Outline each blood parasite and name the species.
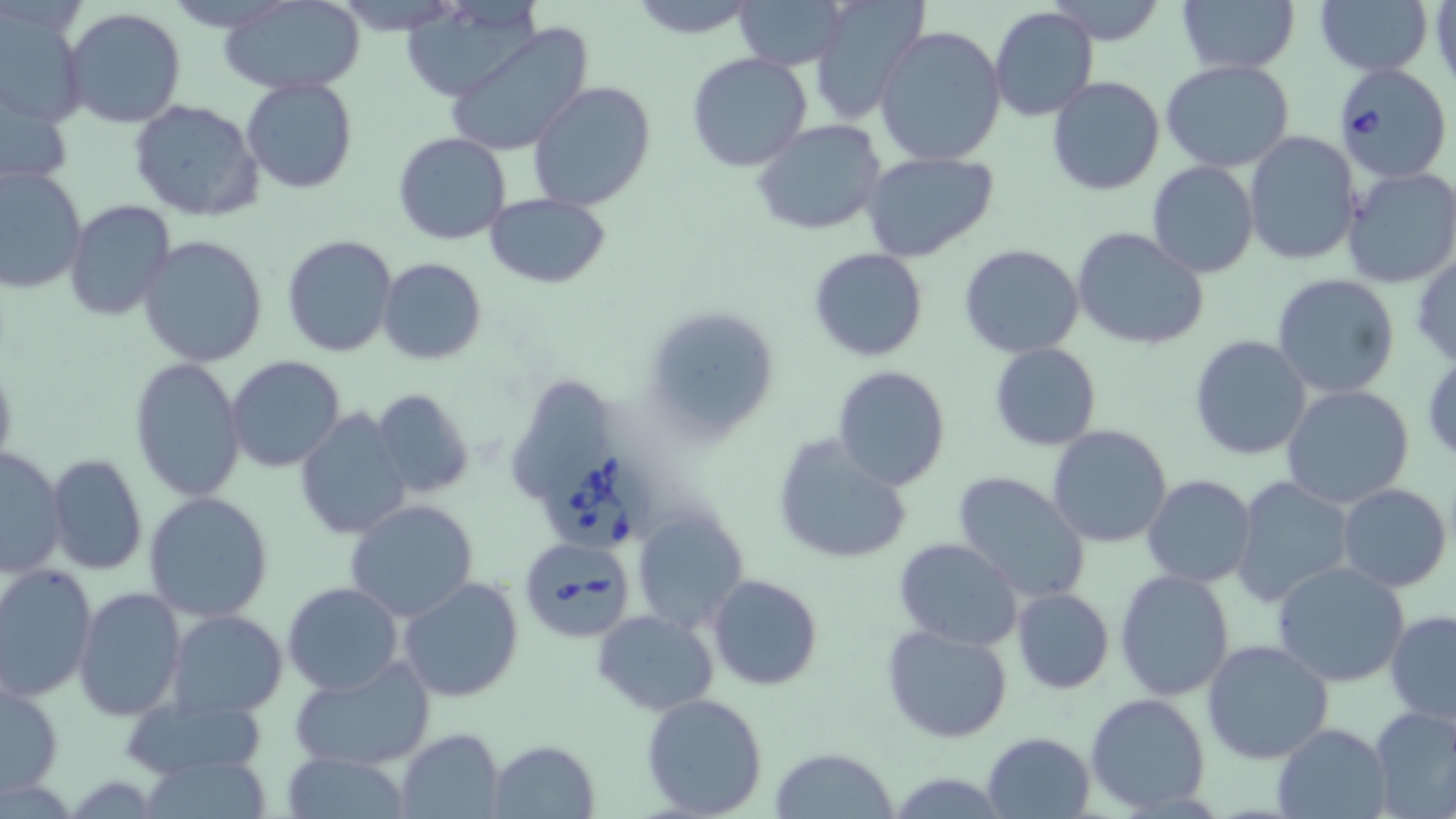
Approximate bounding boxes as named x1/y1/x2/y2 corners in pixels.
Babesia divergens-infected red blood cells: (x1=1335, y1=64, x2=1451, y2=181), (x1=537, y1=451, x2=646, y2=554), (x1=516, y1=534, x2=636, y2=642).
No Plasmodium falciparum, Plasmodium ovale, Plasmodium malariae, Plasmodium vivax, or Trypanosoma brucei observed.

slide-level diagnosis = Babesia divergens
uninfected red blood cell locations = approximate bounding boxes as named x1/y1/x2/y2 corners in pixels: (x1=168, y1=0, x2=289, y2=31), (x1=220, y1=0, x2=366, y2=94), (x1=623, y1=0, x2=762, y2=38), (x1=734, y1=0, x2=844, y2=70), (x1=1047, y1=0, x2=1168, y2=45), (x1=1176, y1=0, x2=1298, y2=74), (x1=397, y1=1, x2=543, y2=102), (x1=1316, y1=1, x2=1433, y2=76), (x1=806, y1=2, x2=928, y2=125), (x1=1, y1=5, x2=89, y2=127), (x1=989, y1=6, x2=1099, y2=124), (x1=62, y1=9, x2=188, y2=130), (x1=444, y1=22, x2=594, y2=156), (x1=874, y1=25, x2=1007, y2=165), (x1=687, y1=52, x2=814, y2=173), (x1=1160, y1=59, x2=1295, y2=171), (x1=0, y1=76, x2=75, y2=194), (x1=1046, y1=76, x2=1166, y2=195), (x1=241, y1=78, x2=358, y2=194), (x1=526, y1=82, x2=657, y2=210), (x1=128, y1=98, x2=265, y2=222), (x1=752, y1=120, x2=888, y2=235), (x1=1244, y1=131, x2=1362, y2=266), (x1=392, y1=133, x2=511, y2=244), (x1=862, y1=151, x2=998, y2=262), (x1=1147, y1=161, x2=1259, y2=279), (x1=0, y1=166, x2=87, y2=296), (x1=1342, y1=167, x2=1456, y2=289), (x1=484, y1=193, x2=613, y2=288), (x1=63, y1=200, x2=175, y2=321), (x1=1071, y1=226, x2=1209, y2=350), (x1=137, y1=234, x2=268, y2=367), (x1=280, y1=234, x2=398, y2=357), (x1=958, y1=243, x2=1085, y2=358), (x1=809, y1=248, x2=928, y2=363), (x1=1410, y1=252, x2=1456, y2=371), (x1=376, y1=257, x2=486, y2=365), (x1=1270, y1=273, x2=1401, y2=399), (x1=643, y1=305, x2=780, y2=442), (x1=1189, y1=335, x2=1312, y2=461), (x1=989, y1=342, x2=1102, y2=451), (x1=227, y1=357, x2=346, y2=474), (x1=130, y1=358, x2=247, y2=503), (x1=0, y1=360, x2=17, y2=474), (x1=831, y1=365, x2=952, y2=491), (x1=1281, y1=383, x2=1414, y2=509), (x1=509, y1=384, x2=612, y2=499), (x1=371, y1=389, x2=476, y2=499), (x1=295, y1=408, x2=412, y2=540), (x1=1047, y1=425, x2=1174, y2=548), (x1=771, y1=434, x2=915, y2=564), (x1=0, y1=446, x2=68, y2=577), (x1=46, y1=452, x2=148, y2=577), (x1=952, y1=471, x2=1091, y2=604), (x1=1141, y1=475, x2=1256, y2=590), (x1=1230, y1=476, x2=1354, y2=608), (x1=1337, y1=483, x2=1452, y2=593), (x1=143, y1=491, x2=274, y2=623), (x1=345, y1=499, x2=479, y2=622), (x1=630, y1=507, x2=749, y2=633), (x1=893, y1=539, x2=1023, y2=650), (x1=1271, y1=561, x2=1409, y2=687), (x1=0, y1=564, x2=97, y2=702), (x1=1115, y1=569, x2=1235, y2=700), (x1=707, y1=574, x2=824, y2=691), (x1=398, y1=576, x2=524, y2=702), (x1=282, y1=582, x2=403, y2=695), (x1=74, y1=586, x2=188, y2=722), (x1=1011, y1=587, x2=1114, y2=694), (x1=592, y1=609, x2=719, y2=715), (x1=167, y1=610, x2=288, y2=719), (x1=1385, y1=611, x2=1456, y2=729), (x1=881, y1=624, x2=1014, y2=744), (x1=1201, y1=639, x2=1334, y2=764), (x1=290, y1=656, x2=437, y2=772), (x1=1, y1=682, x2=65, y2=797), (x1=1087, y1=692, x2=1209, y2=814), (x1=641, y1=693, x2=769, y2=818), (x1=120, y1=696, x2=268, y2=778), (x1=1368, y1=704, x2=1456, y2=818), (x1=1273, y1=722, x2=1392, y2=818), (x1=395, y1=728, x2=504, y2=817), (x1=982, y1=731, x2=1094, y2=817), (x1=486, y1=739, x2=600, y2=818), (x1=768, y1=749, x2=898, y2=819), (x1=283, y1=751, x2=411, y2=818), (x1=138, y1=757, x2=277, y2=816)
field of view = single
modality = light microscopy
preparation = thin blood film
image size = 1456×819 pixels
stain = May-Grünwald-Giemsa
magnification = 1000x